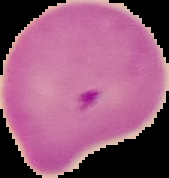 From a thin blood smear. Result: malaria parasites identified. Cell region segmented out of the field of view; the surrounding area is masked to black. Image is 169×178 pixels.